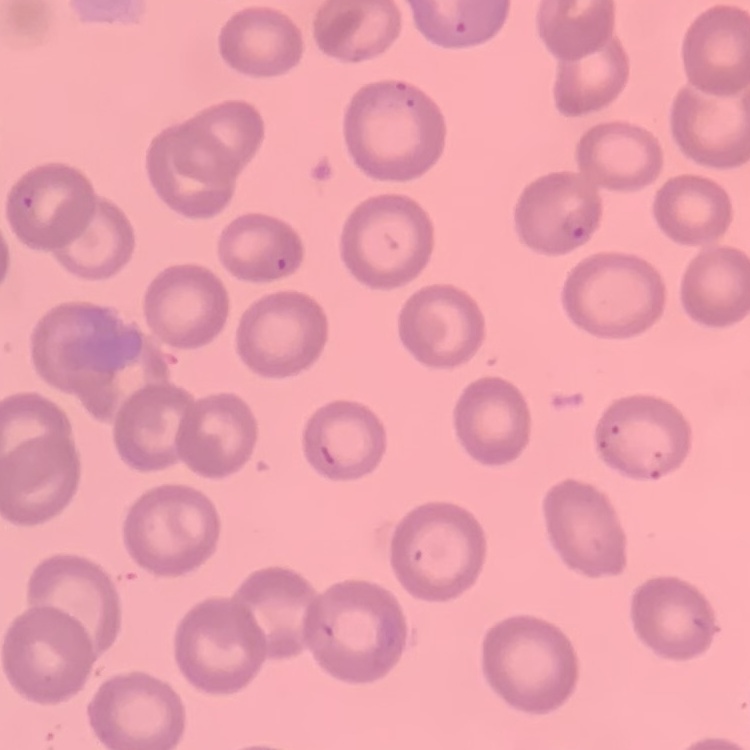

red blood cell morphology = no rouleaux formation
image type = square crop of a larger photomicrograph
stain = Field's or Giemsa
preparation = thin blood smear